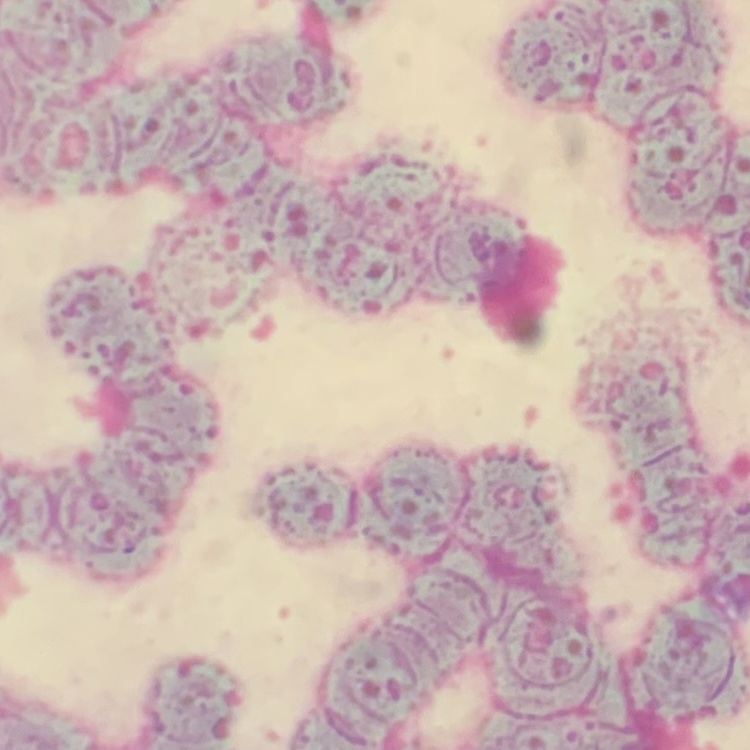 The red blood cells show rouleaux formation. Stained with either Field's or Giemsa. Thin peripheral smear. Square crop of a larger photomicrograph.